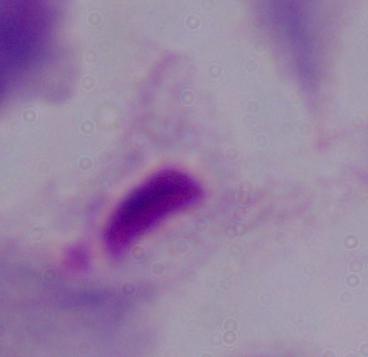
1000x magnification. A trichomonad is shown. Micrograph.